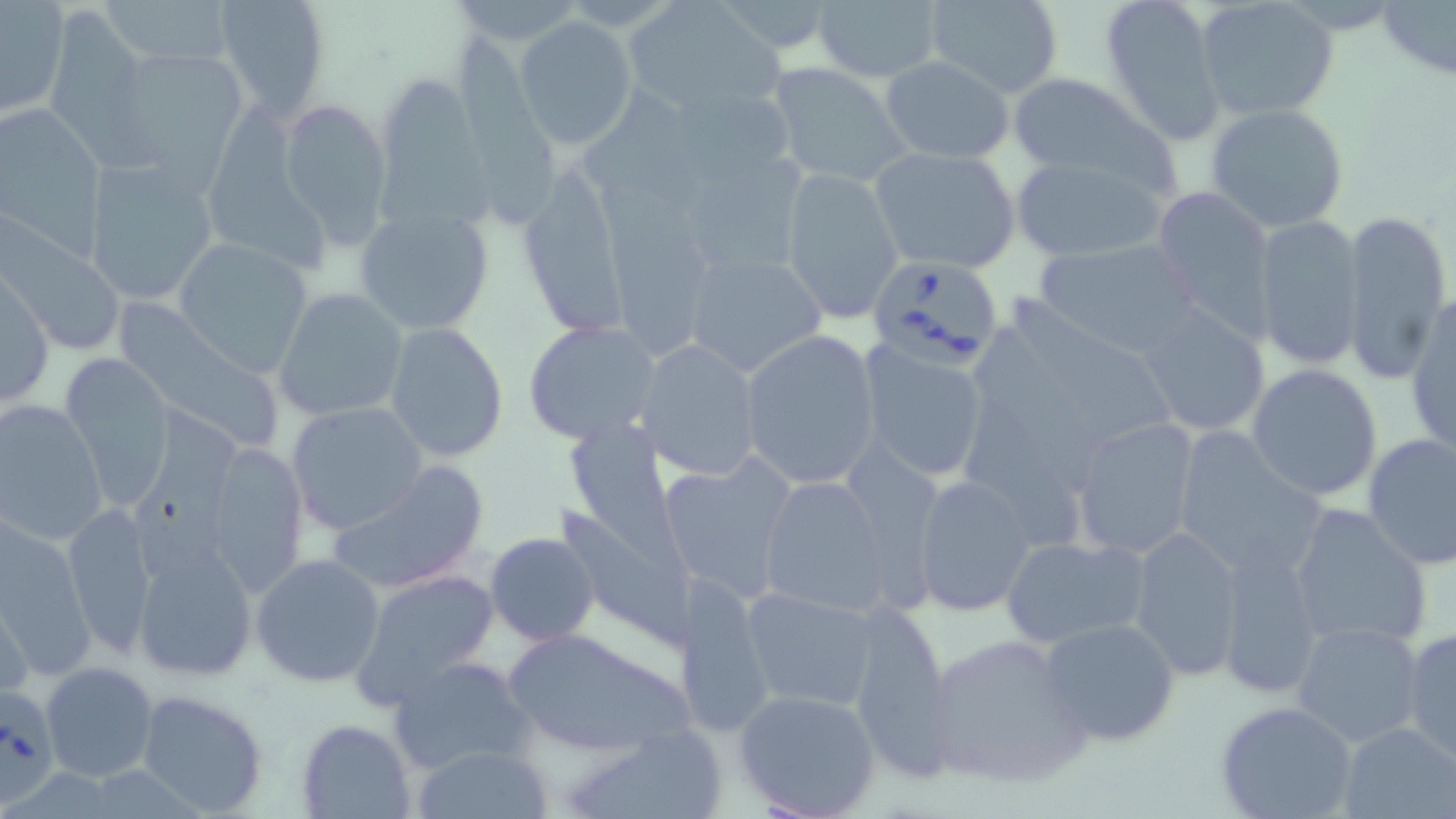 Approximate bounding boxes as (x1, y1, x2, y2) in pixels. Uninfected red blood cell locations: (102, 0, 239, 67), (211, 0, 332, 117), (447, 0, 586, 51), (811, 0, 945, 84), (921, 0, 1064, 97), (1099, 0, 1229, 145), (1194, 0, 1338, 122), (624, 1, 786, 117), (1377, 1, 1456, 77), (37, 3, 168, 175), (1, 4, 69, 116), (514, 15, 639, 151), (453, 27, 569, 221), (104, 45, 249, 179), (880, 55, 1015, 163), (765, 62, 913, 189), (1006, 73, 1169, 187), (373, 80, 504, 225), (278, 96, 393, 245), (1205, 102, 1351, 234), (194, 106, 337, 277), (2, 107, 109, 256), (870, 146, 1021, 274), (691, 150, 818, 269), (1010, 154, 1170, 262), (83, 157, 217, 306), (514, 161, 629, 336), (780, 165, 903, 323), (601, 183, 713, 363), (1151, 183, 1277, 340), (355, 205, 494, 333), (1341, 209, 1451, 384), (1252, 214, 1365, 371), (3, 215, 127, 354), (175, 234, 317, 376), (1031, 237, 1205, 359), (681, 249, 826, 379), (0, 273, 54, 411), (275, 289, 407, 421), (1406, 293, 1456, 455), (1016, 296, 1181, 444), (116, 298, 285, 447), (1138, 305, 1272, 437), (522, 320, 660, 446), (384, 322, 509, 461), (739, 328, 882, 489), (981, 331, 1099, 487), (637, 340, 762, 479), (861, 342, 992, 482), (60, 355, 175, 505), (1246, 364, 1384, 501), (960, 383, 1090, 542), (1, 399, 110, 549), (135, 400, 241, 573), (286, 401, 427, 535), (572, 416, 703, 579), (1070, 418, 1202, 560), (1173, 427, 1326, 579), (1362, 432, 1456, 569), (206, 439, 310, 597), (658, 452, 796, 601), (328, 460, 489, 592), (753, 470, 912, 620), (911, 474, 1037, 618), (1287, 502, 1433, 649), (63, 503, 159, 658), (560, 504, 698, 660), (0, 517, 91, 675), (1128, 525, 1247, 680), (485, 532, 599, 645), (1000, 537, 1150, 649), (131, 541, 261, 682), (1214, 543, 1323, 697), (251, 554, 386, 688), (348, 568, 499, 706), (674, 576, 776, 737), (741, 586, 882, 710), (0, 592, 32, 704), (845, 605, 955, 773), (1039, 616, 1180, 747), (1292, 620, 1427, 748), (1401, 625, 1456, 765), (501, 627, 698, 757), (925, 631, 1092, 789), (387, 656, 536, 774), (41, 662, 160, 783), (137, 687, 271, 816), (734, 688, 882, 818), (1215, 701, 1358, 819), (296, 718, 415, 819), (1338, 720, 1456, 819), (573, 728, 728, 819), (412, 744, 554, 818). Babesia divergens-infected red blood cell locations: (865, 255, 1007, 367), (0, 689, 61, 806). Slide-level diagnosis: Babesia divergens. Optical microscopy. Image is 1456×819 pixels. 1000x magnification. Thin blood film. One field of a larger specimen. May-Grünwald-Giemsa stain.